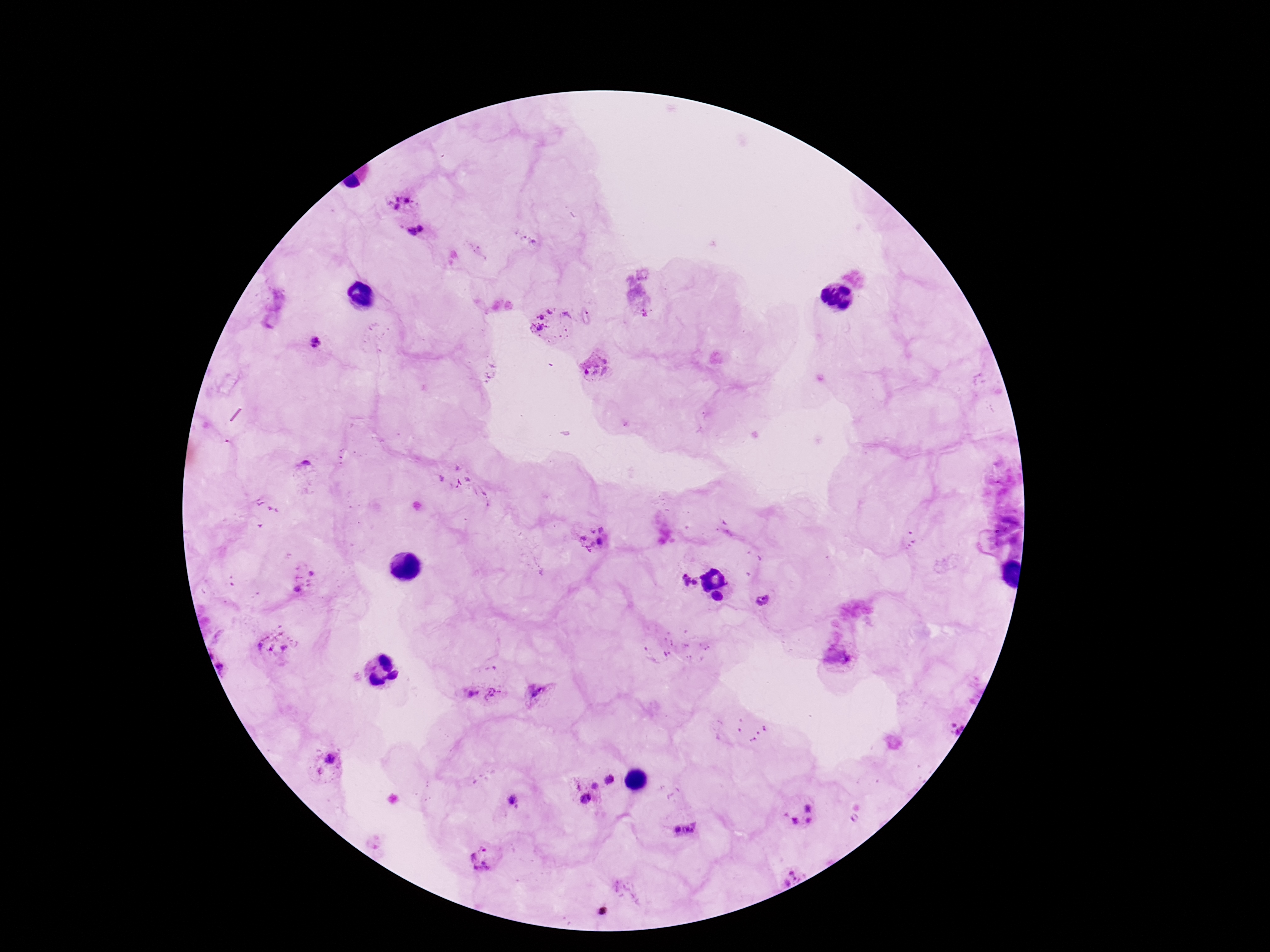
stain = Giemsa
image size = 1270×952 pixels
preparation = thick blood film
magnification = 100x
Plasmodium parasite locations = approximate centers as (x, y) in pixels: (404, 198), (417, 232), (554, 323), (315, 343), (596, 363), (597, 542), (302, 579), (682, 584), (762, 596), (275, 643), (840, 657), (538, 692), (480, 694), (328, 765), (613, 779), (580, 794), (512, 800), (797, 812), (686, 830), (483, 858), (789, 874)
patient malaria status = positive
field of view = single
capture = smartphone camera through the microscope eyepiece